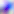
Summary:
  - Magnification: 400x
  - Modality: micrograph
  - Identification: Toxoplasma gondii